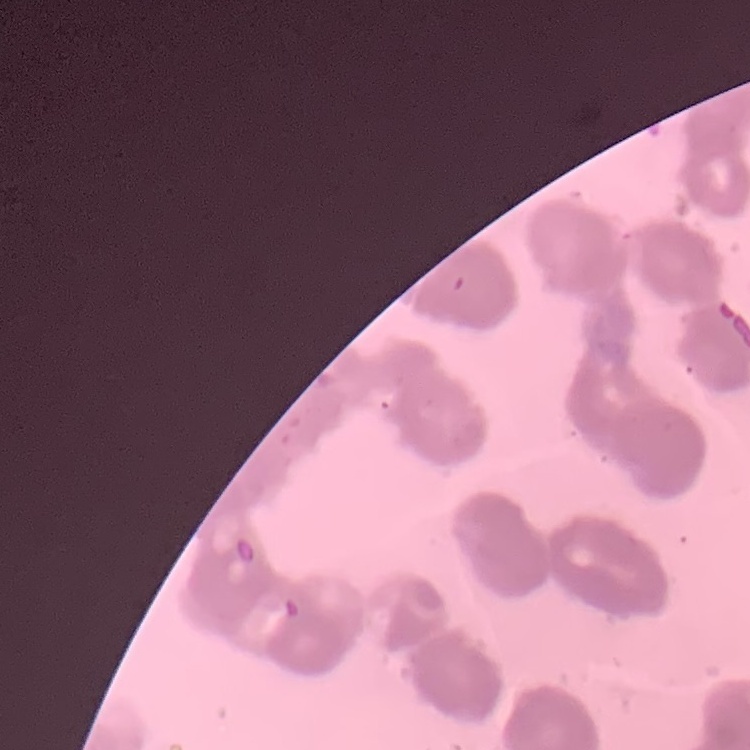

Summary:
  - Red blood cell morphology: rouleaux formation
  - Image type: one tile cut from a larger photomicrograph
  - Preparation: thin blood film
  - Stain: Field's or Giemsa